Comment on the morphology of the erythrocytes.
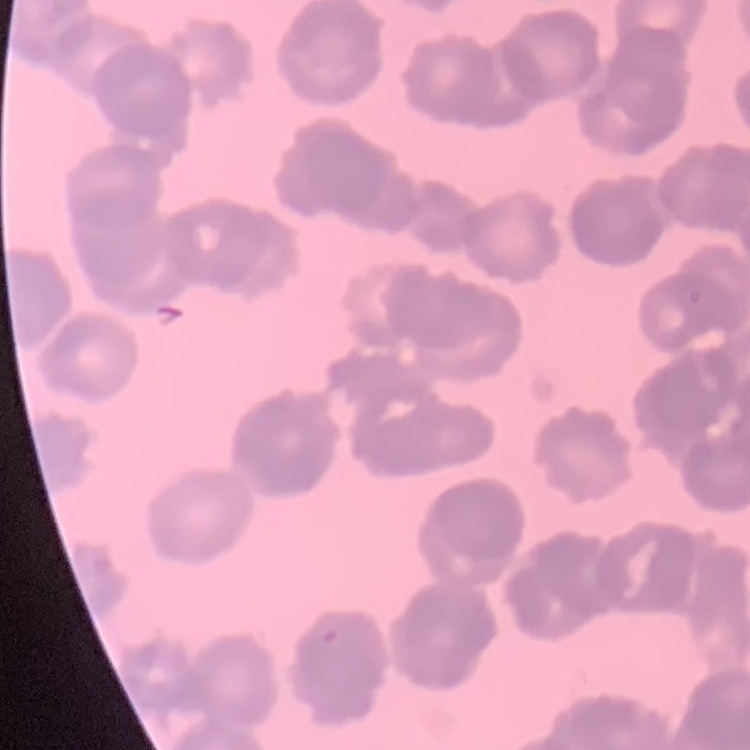

They show rouleaux formation.

image type = square crop of a larger photomicrograph
preparation = thin blood smear
stain = Field's or Giemsa